Classify this cell by malaria status.
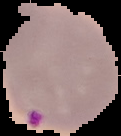
Parasitized.

Summary:
  - Image size: 121×136 pixels
  - Image type: cell region segmented out of the field of view; surrounding area masked to black
  - Preparation: thin blood smear